Assess the morphology of the red blood cells.
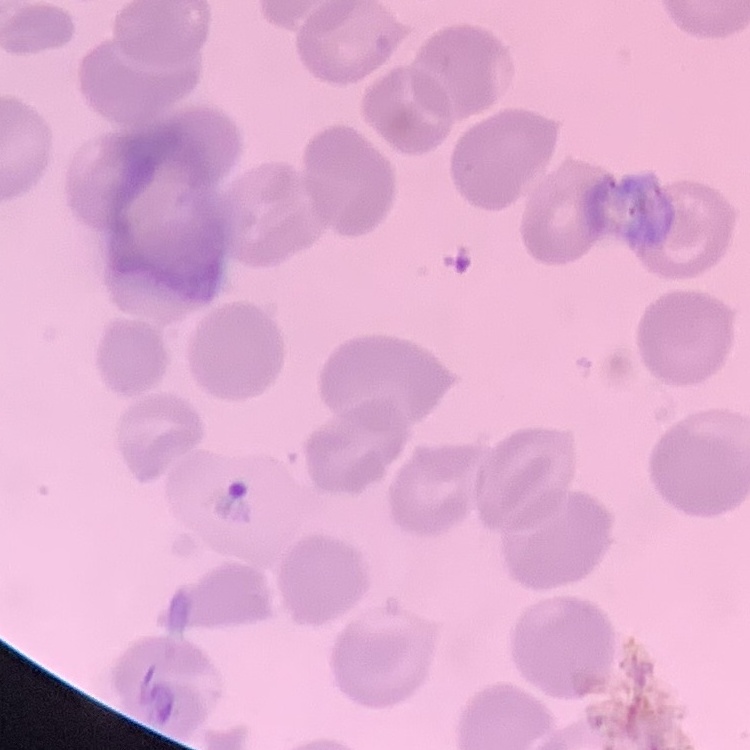

They show no rouleaux formation.

Stained with either Field's or Giemsa. Thin blood smear. One tile cut from a larger photomicrograph.